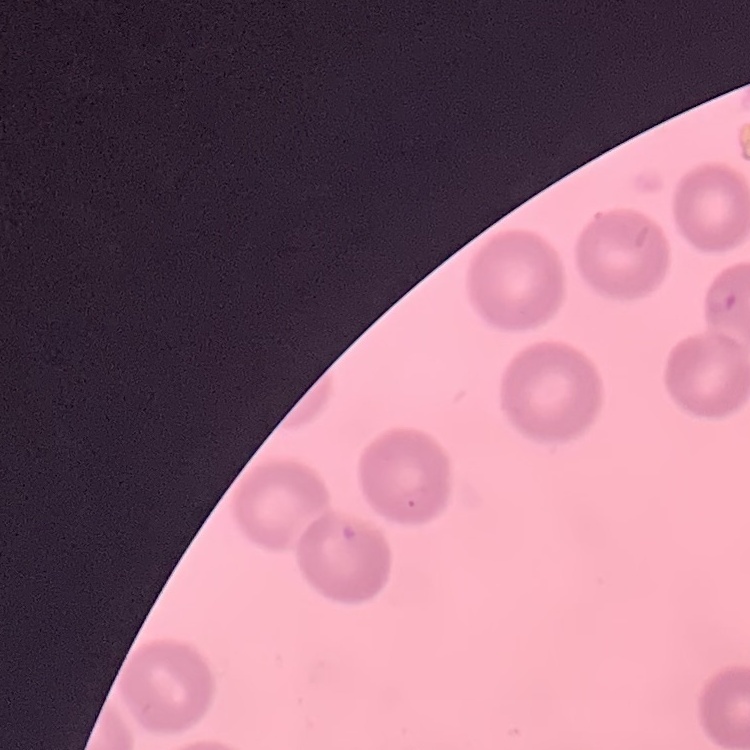

red blood cell morphology = no rouleaux formation
image type = one tile cut from a larger photomicrograph
preparation = thin peripheral smear
stain = Field's or Giemsa